Outline each Plasmodium falciparum-infected red blood cell.
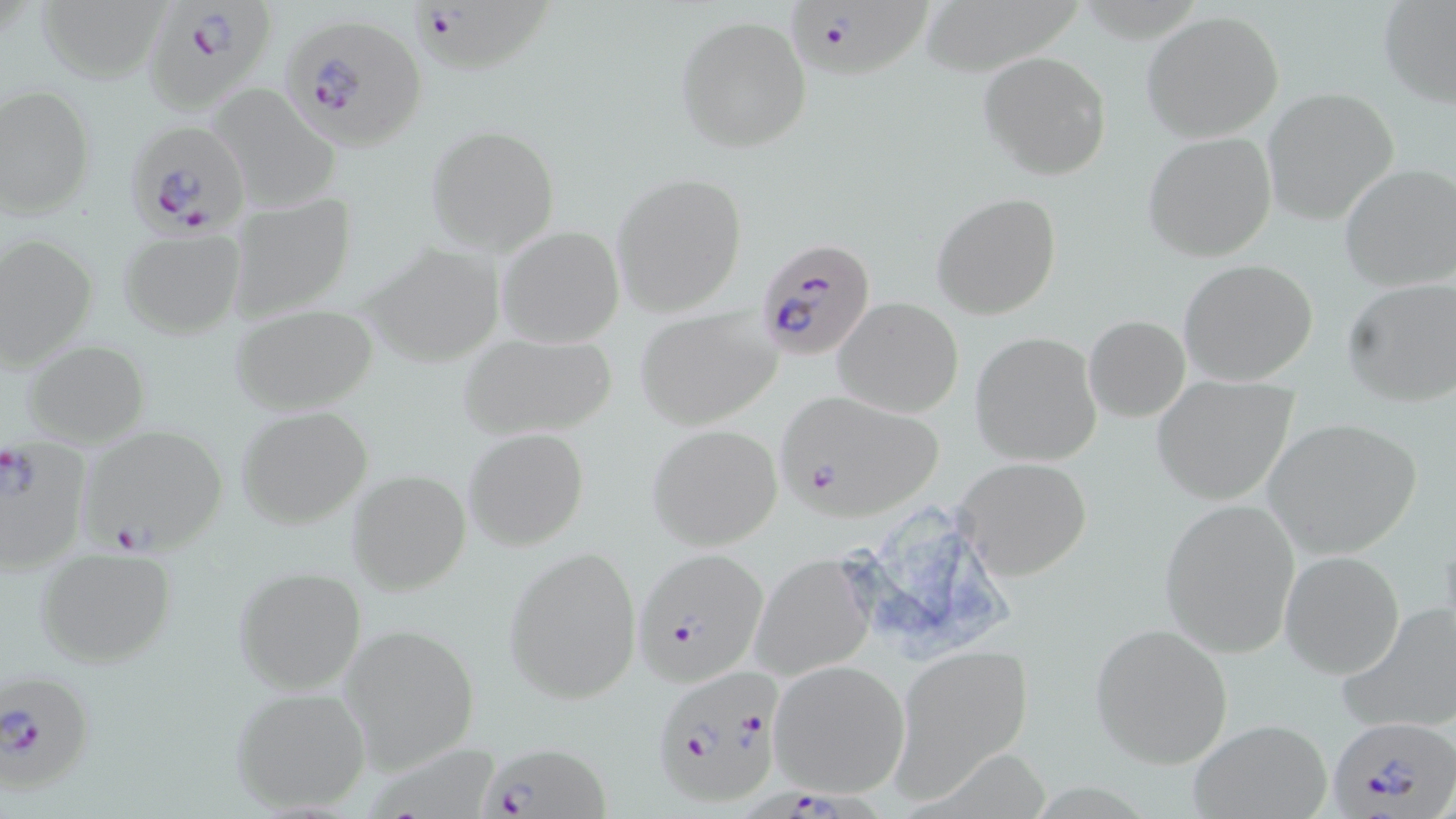
Approximate bounding boxes as [x1, y1, x2, y2] in pixels.
Plasmodium falciparum-infected red blood cells: [149, 1, 273, 121], [410, 1, 559, 75], [788, 1, 933, 78], [284, 23, 430, 159], [118, 120, 246, 240], [751, 234, 877, 360], [778, 388, 947, 520], [79, 425, 228, 554], [0, 438, 88, 576], [634, 544, 770, 689], [652, 667, 786, 807], [1, 669, 97, 794], [1327, 716, 1456, 818], [476, 741, 611, 819], [737, 784, 902, 818].

Summary:
  - Uninfected red blood cell locations: [37, 0, 178, 86], [924, 0, 1089, 76], [1378, 1, 1456, 108], [1141, 10, 1284, 143], [675, 15, 812, 154], [979, 52, 1112, 180], [208, 84, 342, 211], [1, 85, 96, 220], [1262, 87, 1399, 226], [426, 125, 560, 255], [1142, 132, 1277, 262], [1339, 165, 1455, 291], [610, 172, 747, 316], [226, 191, 359, 323], [931, 192, 1062, 321], [497, 226, 625, 348], [117, 229, 245, 340], [0, 234, 100, 368], [357, 243, 507, 369], [1179, 259, 1320, 387], [1342, 277, 1456, 408], [834, 297, 964, 418], [230, 304, 378, 414], [633, 305, 783, 427], [1084, 316, 1190, 423], [454, 331, 619, 442], [970, 331, 1104, 467], [22, 341, 151, 445], [1151, 376, 1300, 507], [235, 405, 373, 529], [1262, 416, 1423, 560], [647, 423, 783, 551], [464, 427, 591, 551], [957, 457, 1092, 580], [347, 470, 471, 595], [1159, 497, 1301, 658], [828, 501, 1023, 670], [33, 545, 177, 669], [504, 546, 642, 702], [1280, 550, 1405, 679], [749, 554, 876, 682], [232, 565, 369, 695], [1341, 606, 1456, 733], [1088, 620, 1235, 768], [340, 624, 480, 772], [894, 644, 1034, 794], [768, 661, 910, 796], [229, 685, 373, 814], [1189, 718, 1334, 819]
  - Slide-level diagnosis: Plasmodium falciparum
  - Field of view: single
  - Stain: May-Grünwald-Giemsa
  - Magnification: 1000x
  - Image size: 1456×819 pixels
  - Preparation: thin blood smear
  - Modality: light microscopy